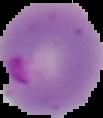

image type = cell region segmented out of the field of view; surrounding area masked to black
image size = 103×118 pixels
preparation = thin blood smear
malaria status = parasitized